Report the malaria status of this cell.
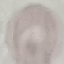
Uninfected.

preparation: thin blood smear
capture: smartphone camera at the microscope eyepiece
stain: Giemsa
image_type: automatically extracted cell patch, resized to 64 × 64 pixels